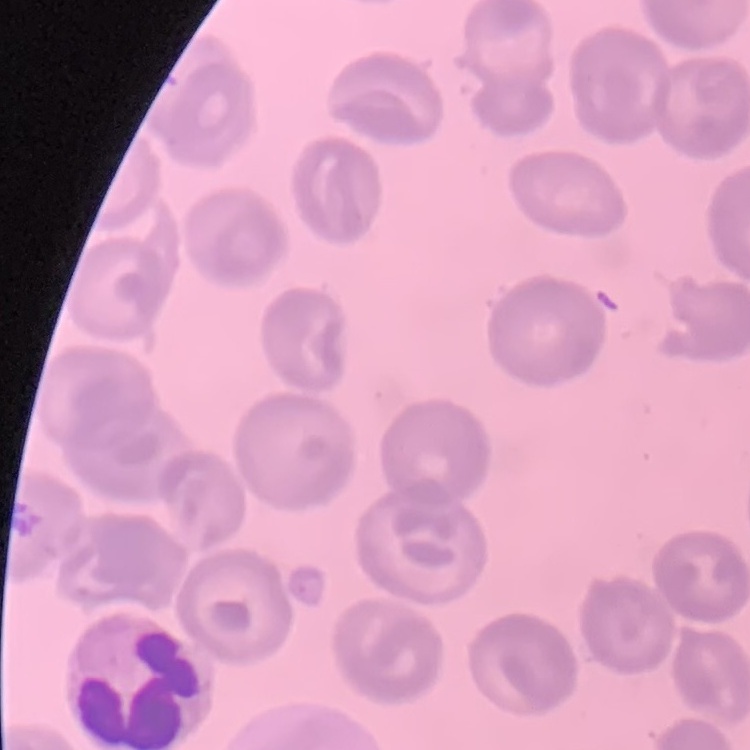 The red blood cells show no rouleaux formation. Stained with either Field's or Giemsa. Square crop of a larger photomicrograph. Thin peripheral smear.